Classify this cell by malaria status.
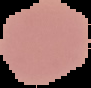
It is uninfected.

Summary:
  - Preparation: thin blood smear
  - Image type: cell region segmented out of the field of view; surrounding area masked to black
  - Image size: 91×88 pixels